Locate every Plasmodium ovale-infected red blood cell.
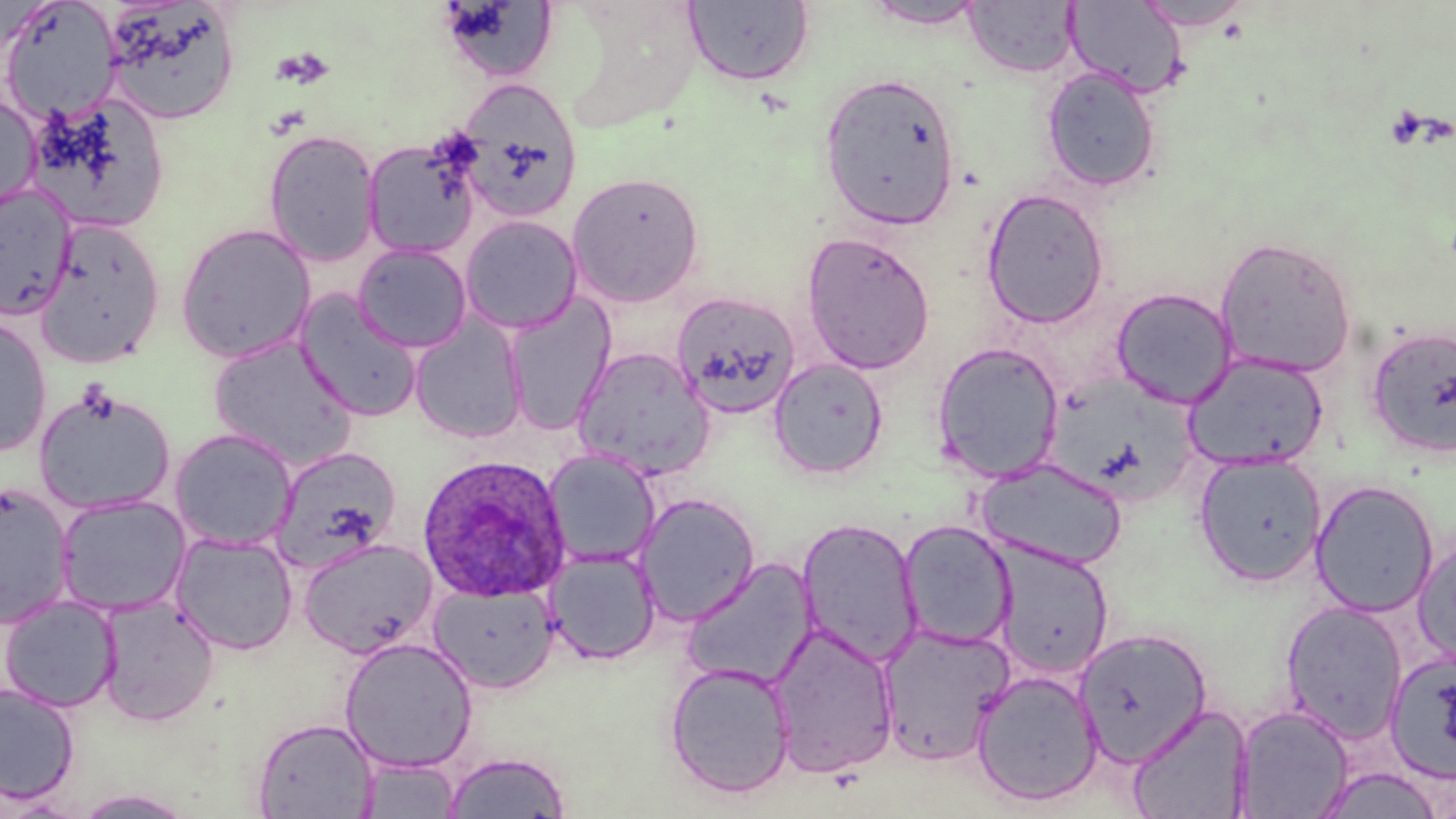

Approximate bounding boxes as named x1/y1/x2/y2 corners in pixels.
Plasmodium ovale-infected red blood cells: (x1=415, y1=454, x2=572, y2=602).

{
  "slide_level_diagnosis": "Plasmodium ovale",
  "stain": "May-Grünwald-Giemsa",
  "image_size": "1456×819 pixels",
  "preparation": "thin blood film",
  "platelet_locations": "approximate bounding boxes as named x1/y1/x2/y2 corners in pixels: (x1=271, y1=47, x2=333, y2=89), (x1=74, y1=382, x2=119, y2=425)",
  "magnification": "1000x",
  "field_of_view": "one of a larger specimen",
  "uninfected_red_blood_cell_locations": "approximate bounding boxes as named x1/y1/x2/y2 corners in pixels: (x1=1, y1=0, x2=121, y2=125), (x1=101, y1=1, x2=240, y2=126), (x1=683, y1=1, x2=815, y2=87), (x1=963, y1=1, x2=1079, y2=77), (x1=1065, y1=1, x2=1188, y2=99), (x1=1133, y1=1, x2=1255, y2=31), (x1=438, y1=2, x2=558, y2=81), (x1=859, y1=2, x2=990, y2=30), (x1=1040, y1=66, x2=1162, y2=193), (x1=818, y1=71, x2=962, y2=230), (x1=455, y1=79, x2=583, y2=224), (x1=0, y1=90, x2=41, y2=213), (x1=24, y1=94, x2=170, y2=235), (x1=263, y1=129, x2=381, y2=266), (x1=362, y1=135, x2=482, y2=259), (x1=567, y1=171, x2=705, y2=307), (x1=0, y1=184, x2=76, y2=320), (x1=981, y1=188, x2=1110, y2=328), (x1=460, y1=215, x2=583, y2=334), (x1=34, y1=219, x2=166, y2=369), (x1=174, y1=223, x2=317, y2=363), (x1=801, y1=232, x2=936, y2=374), (x1=1214, y1=235, x2=1357, y2=378), (x1=353, y1=243, x2=473, y2=352), (x1=1111, y1=287, x2=1238, y2=408), (x1=671, y1=291, x2=801, y2=419), (x1=295, y1=292, x2=424, y2=421), (x1=503, y1=295, x2=615, y2=434), (x1=410, y1=314, x2=528, y2=444), (x1=0, y1=315, x2=53, y2=457), (x1=1365, y1=324, x2=1456, y2=459), (x1=208, y1=336, x2=358, y2=471), (x1=931, y1=342, x2=1065, y2=482), (x1=572, y1=347, x2=715, y2=480), (x1=1183, y1=353, x2=1329, y2=471), (x1=768, y1=359, x2=888, y2=480), (x1=33, y1=387, x2=176, y2=515), (x1=169, y1=427, x2=297, y2=552), (x1=271, y1=446, x2=402, y2=572), (x1=542, y1=449, x2=661, y2=568), (x1=1193, y1=453, x2=1327, y2=586), (x1=977, y1=457, x2=1128, y2=571), (x1=1310, y1=480, x2=1439, y2=617), (x1=0, y1=482, x2=75, y2=628), (x1=634, y1=493, x2=761, y2=625), (x1=55, y1=494, x2=191, y2=617), (x1=795, y1=517, x2=924, y2=668), (x1=898, y1=519, x2=1017, y2=650), (x1=170, y1=532, x2=298, y2=655), (x1=1413, y1=535, x2=1456, y2=668), (x1=297, y1=538, x2=439, y2=658), (x1=991, y1=540, x2=1115, y2=680), (x1=545, y1=548, x2=661, y2=665), (x1=681, y1=557, x2=820, y2=690), (x1=428, y1=582, x2=559, y2=693), (x1=0, y1=595, x2=121, y2=712), (x1=96, y1=596, x2=220, y2=726), (x1=1280, y1=600, x2=1409, y2=742), (x1=766, y1=622, x2=900, y2=778), (x1=875, y1=622, x2=1015, y2=765), (x1=1073, y1=627, x2=1211, y2=766), (x1=339, y1=637, x2=479, y2=773), (x1=1384, y1=650, x2=1456, y2=784), (x1=663, y1=661, x2=797, y2=799), (x1=970, y1=670, x2=1104, y2=807), (x1=0, y1=682, x2=79, y2=805), (x1=1127, y1=702, x2=1255, y2=819), (x1=1232, y1=704, x2=1356, y2=818), (x1=251, y1=717, x2=378, y2=818), (x1=442, y1=750, x2=572, y2=818), (x1=356, y1=757, x2=462, y2=818), (x1=1316, y1=767, x2=1444, y2=818), (x1=72, y1=789, x2=196, y2=818), (x1=0, y1=793, x2=91, y2=817)",
  "modality": "optical microscopy"
}